Report the malaria status.
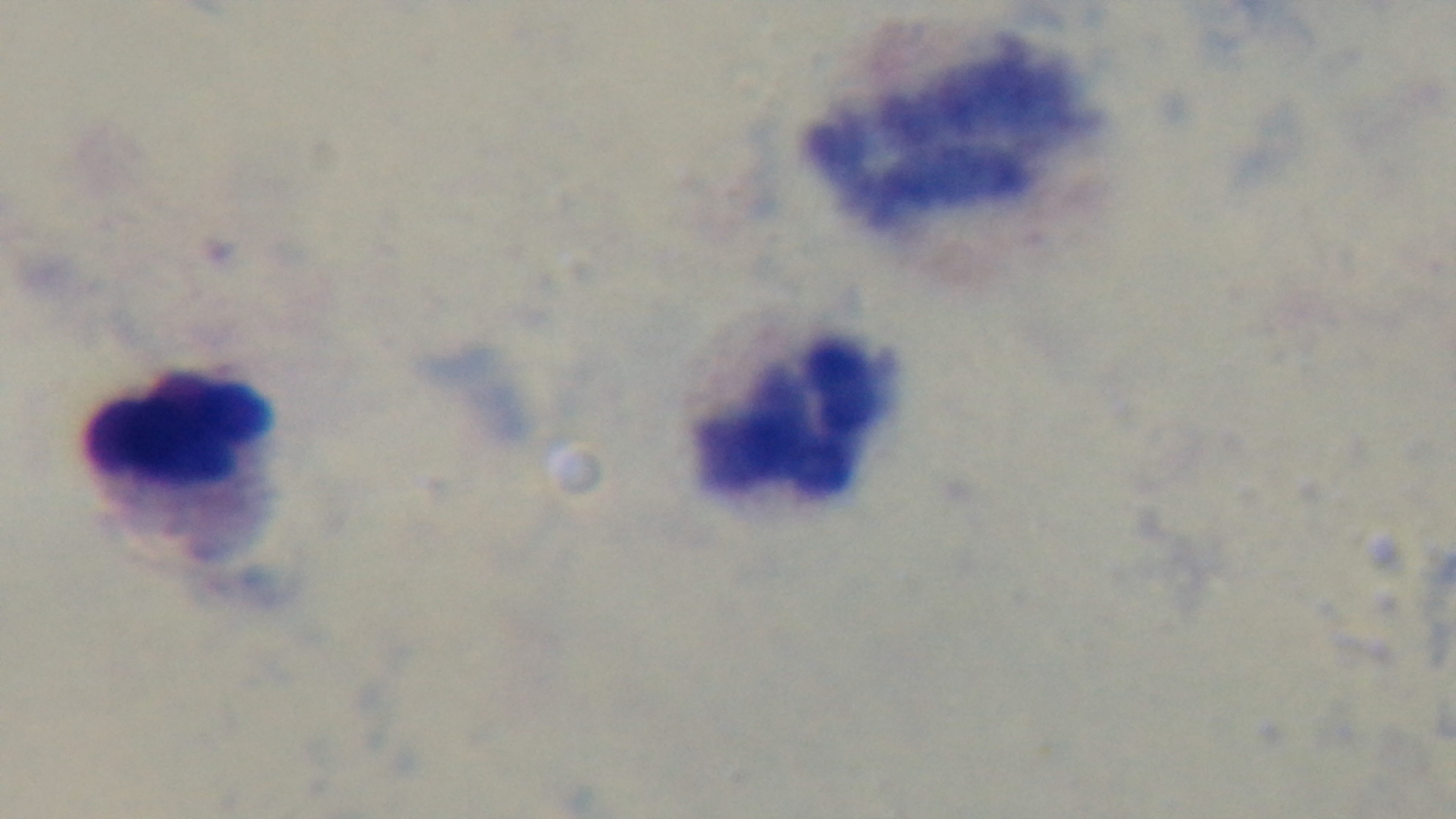

Negative.

Giemsa stain. Light microscopy. Preparation: thick blood film. One field from the slide. 100x oil-immersion objective. Mounted 4K digital camera.